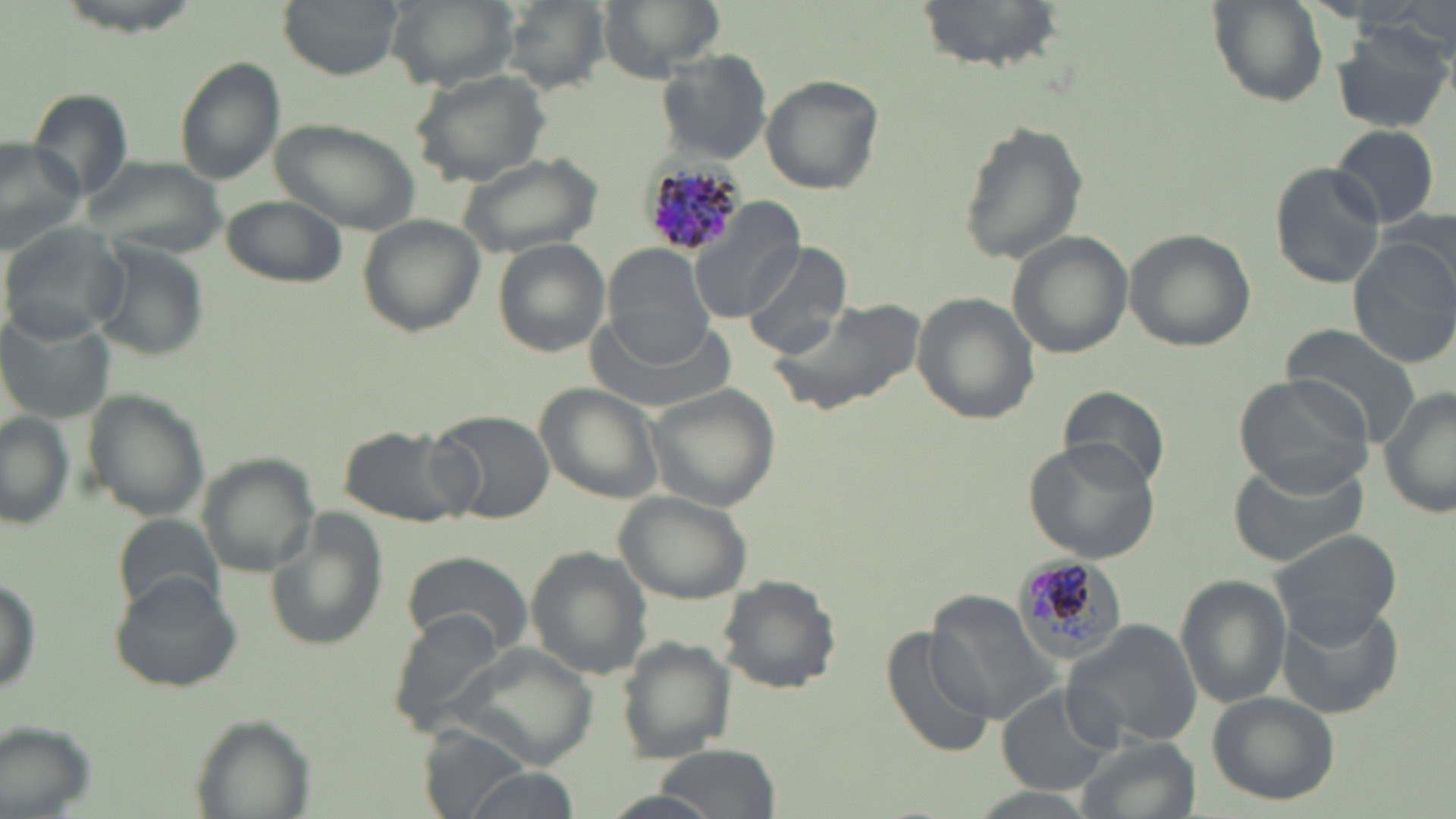

{
  "slide_level_diagnosis": "Plasmodium malariae",
  "image_size": "1456×819 pixels",
  "magnification": "1000x",
  "uninfected_red_blood_cell_locations": "approximate bounding boxes as (x1,y1)-(x2,y2) corner pairs in pixels: (277,0)-(404,77), (383,0)-(520,89), (500,0)-(612,92), (598,0)-(725,78), (919,0)-(1066,69), (1208,1)-(1327,107), (1332,24)-(1451,134), (655,48)-(772,164), (175,58)-(285,187), (411,67)-(553,186), (761,75)-(883,194), (27,88)-(135,201), (271,117)-(420,234), (957,120)-(1088,265), (1330,123)-(1442,229), (0,138)-(86,255), (454,151)-(605,260), (83,158)-(225,258), (1269,162)-(1386,289), (221,194)-(346,288), (690,202)-(805,324), (359,216)-(483,335), (1,223)-(130,342), (1124,229)-(1254,352), (1007,233)-(1132,359), (1348,234)-(1456,368), (494,238)-(611,358), (94,240)-(210,363), (741,241)-(853,360), (607,246)-(718,366), (1313,250)-(1434,405), (911,293)-(1038,424), (771,298)-(928,419), (587,307)-(733,419), (3,309)-(117,421), (1283,324)-(1424,448), (1234,371)-(1376,496), (1062,382)-(1174,491), (539,385)-(665,502), (1379,386)-(1455,521), (648,387)-(779,512), (81,389)-(210,521), (431,409)-(556,524), (0,413)-(75,529), (347,426)-(476,527), (1022,439)-(1162,562), (197,453)-(320,578), (1228,457)-(1373,565), (615,490)-(753,602), (262,509)-(388,655), (114,514)-(225,618), (1270,528)-(1405,643), (529,548)-(654,678), (402,549)-(532,655), (0,570)-(41,702), (108,572)-(245,693), (1176,574)-(1289,708), (719,575)-(841,693), (926,589)-(1064,726), (1278,602)-(1402,719), (389,611)-(509,733), (1063,620)-(1206,751), (882,625)-(996,759), (617,638)-(737,763), (456,646)-(597,766), (997,686)-(1116,796), (1205,690)-(1340,804), (186,715)-(314,818), (1075,736)-(1199,819), (650,746)-(780,819), (458,770)-(582,819), (959,787)-(1104,818)",
  "stain": "May-Grünwald-Giemsa",
  "preparation": "thin blood film",
  "modality": "light microscopy",
  "plasmodium_malariae_infected_red_blood_cell_locations": "approximate bounding boxes as (x1,y1)-(x2,y2) corner pairs in pixels: (641,159)-(746,261), (1009,555)-(1118,662)",
  "field_of_view": "one of a larger specimen"
}